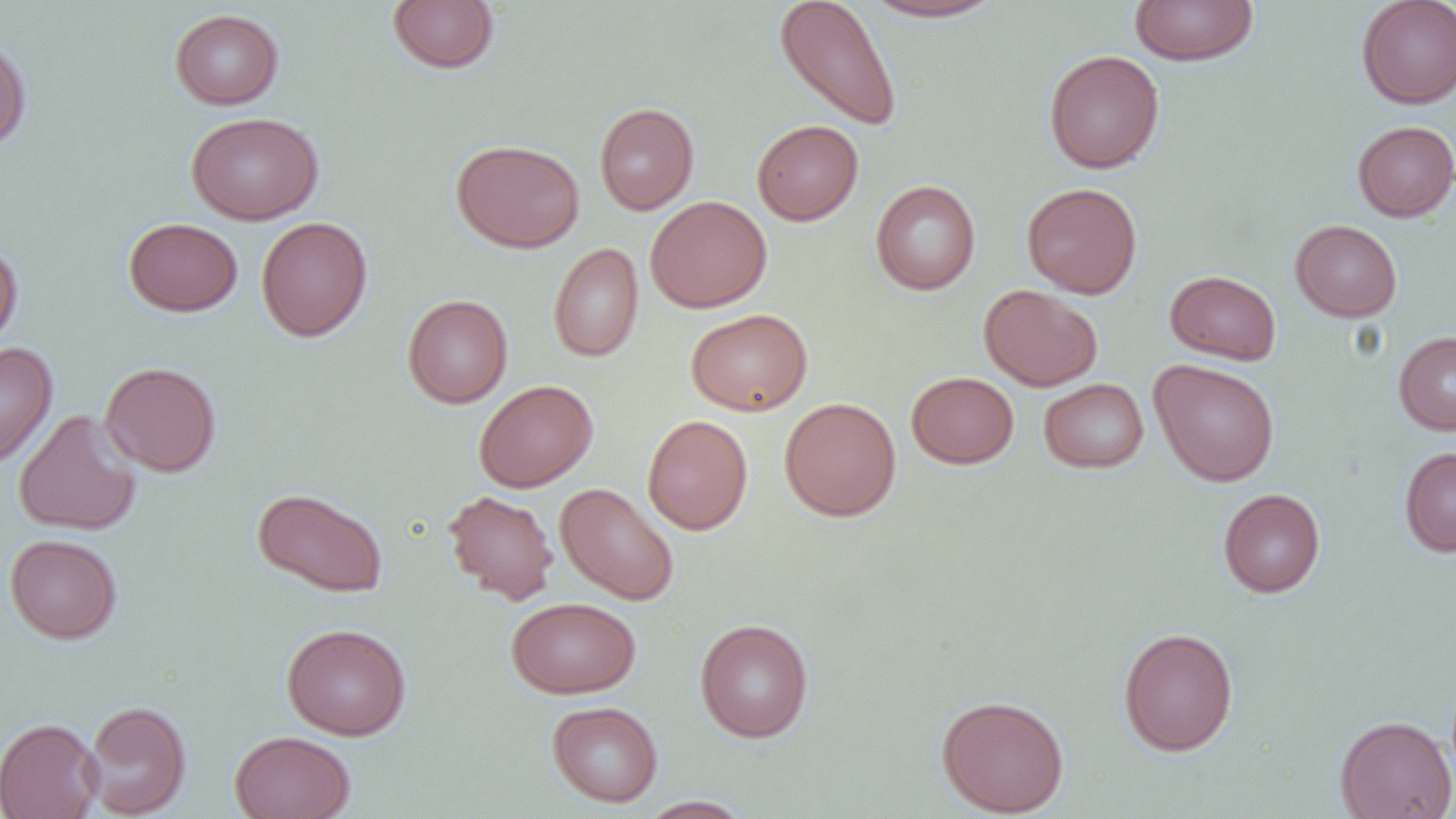

Summary:
  - Coordinate format: approximate bounding boxes as [x1, y1, x2, y2] in pixels
  - Uninfected red blood cell locations: [387, 0, 499, 74], [774, 0, 903, 132], [859, 0, 1008, 23], [1129, 0, 1259, 66], [1356, 0, 1456, 109], [169, 8, 284, 109], [0, 34, 32, 153], [1044, 50, 1165, 173], [594, 102, 699, 215], [185, 111, 323, 224], [751, 119, 863, 225], [1352, 120, 1456, 222], [451, 139, 584, 253], [870, 179, 981, 295], [1022, 182, 1142, 299], [644, 195, 773, 313], [256, 216, 372, 341], [123, 217, 243, 316], [1290, 219, 1402, 321], [0, 241, 23, 353], [549, 243, 644, 362], [1165, 270, 1282, 365], [979, 284, 1103, 391], [402, 294, 513, 408], [686, 308, 812, 415], [1393, 331, 1456, 434], [0, 342, 57, 468], [1149, 358, 1280, 487], [99, 361, 222, 477], [906, 371, 1019, 469], [1039, 378, 1148, 473], [473, 379, 598, 493], [779, 397, 901, 522], [13, 410, 141, 536], [642, 415, 753, 534], [1399, 446, 1456, 557], [555, 482, 679, 605], [251, 487, 388, 598], [1218, 488, 1326, 597], [442, 489, 559, 605], [4, 533, 122, 644], [506, 597, 640, 699], [694, 618, 814, 743], [281, 623, 412, 741], [1118, 626, 1238, 756], [936, 694, 1069, 816], [83, 700, 191, 818], [547, 701, 663, 807], [1334, 715, 1455, 819], [0, 717, 102, 819], [230, 730, 356, 819], [637, 796, 755, 818]
  - Slide-level diagnosis: negative for blood parasites
  - Image size: 1456×819 pixels
  - Magnification: 1000x
  - Field of view: single
  - Preparation: thin blood film
  - Modality: light microscopy